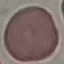 Result: no malaria parasites detected. Giemsa-stained preparation. Thin blood smear. Photographed with a smartphone camera at the microscope eyepiece. Automatically extracted cell patch, resized to 64 × 64 pixels.